Outline each uninfected red blood cell.
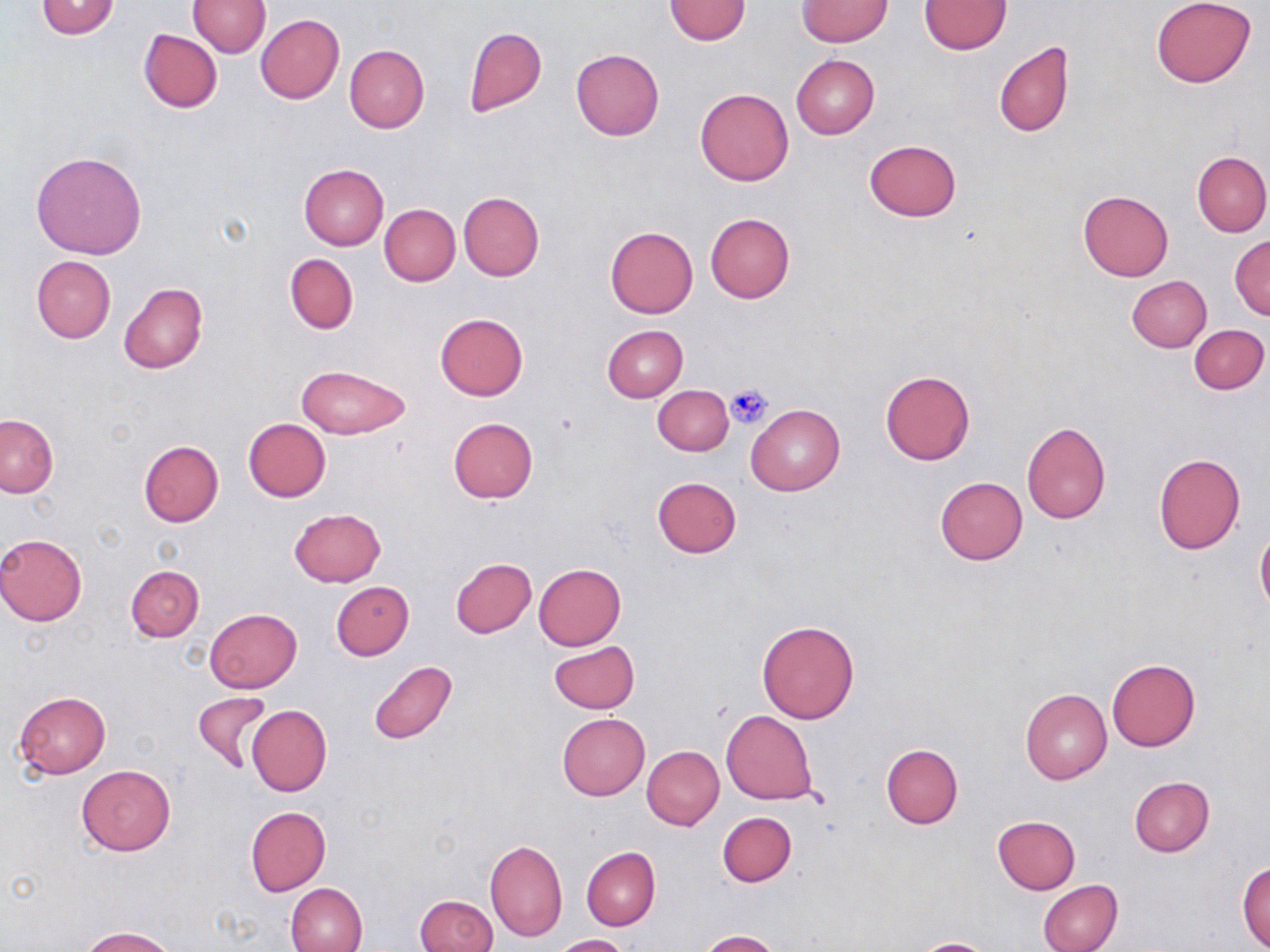

Approximate bounding boxes as (x1, y1, x2, y2) in pixels.
Uninfected red blood cells: (664, 0, 751, 46), (1151, 0, 1257, 88), (35, 1, 121, 40), (189, 1, 269, 56), (797, 1, 891, 47), (920, 1, 1011, 54), (255, 14, 345, 104), (463, 26, 546, 118), (138, 28, 222, 112), (993, 41, 1076, 138), (344, 45, 429, 133), (571, 49, 665, 140), (791, 54, 879, 138), (694, 88, 794, 186), (863, 139, 962, 221), (30, 150, 147, 259), (1192, 152, 1270, 237), (298, 163, 389, 250), (1078, 189, 1174, 280), (458, 192, 544, 282), (379, 204, 460, 286), (705, 212, 794, 304), (606, 225, 698, 318), (1230, 236, 1270, 319), (285, 254, 358, 334), (32, 256, 115, 343), (1127, 276, 1212, 351), (118, 282, 207, 375), (434, 313, 528, 399), (602, 324, 688, 402), (1189, 324, 1268, 394), (295, 363, 411, 439), (879, 369, 975, 465), (654, 384, 734, 455), (746, 403, 844, 496), (0, 415, 57, 498), (243, 417, 331, 501), (448, 417, 538, 503), (1022, 421, 1111, 524), (137, 439, 223, 528), (1153, 454, 1245, 554), (935, 476, 1028, 564), (651, 477, 741, 558), (289, 508, 385, 587), (1255, 532, 1270, 615), (0, 533, 87, 626), (450, 558, 537, 638), (533, 563, 626, 650), (126, 565, 203, 641), (330, 581, 413, 660), (205, 608, 301, 692), (757, 618, 861, 723), (549, 641, 639, 715), (1107, 658, 1200, 750), (367, 660, 457, 746), (1020, 688, 1112, 784), (192, 690, 272, 773), (14, 691, 110, 778), (247, 705, 332, 796), (721, 710, 818, 804), (557, 713, 650, 801), (881, 745, 963, 828), (642, 746, 725, 830), (76, 765, 174, 855), (1129, 777, 1215, 857), (246, 806, 331, 896), (717, 811, 797, 886), (992, 816, 1080, 894), (486, 840, 567, 942), (582, 847, 661, 930), (1237, 860, 1270, 950), (1038, 879, 1122, 952), (285, 882, 367, 952), (416, 894, 497, 952), (82, 926, 177, 952), (697, 930, 781, 952), (553, 934, 633, 952), (909, 938, 999, 951).

{
  "slide_level_diagnosis": "no evidence of blood parasites",
  "image_size": "1270×952 pixels",
  "stain": "May-Grünwald-Giemsa",
  "magnification": "1000x",
  "modality": "optical microscopy",
  "preparation": "thin blood film",
  "field_of_view": "one of a larger specimen",
  "platelet_locations": "approximate bounding boxes as (x1, y1, x2, y2) in pixels: (726, 384, 774, 429)"
}